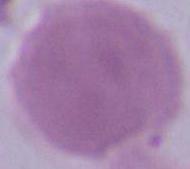
An erythrocyte is shown. 1000x magnification. Micrograph.